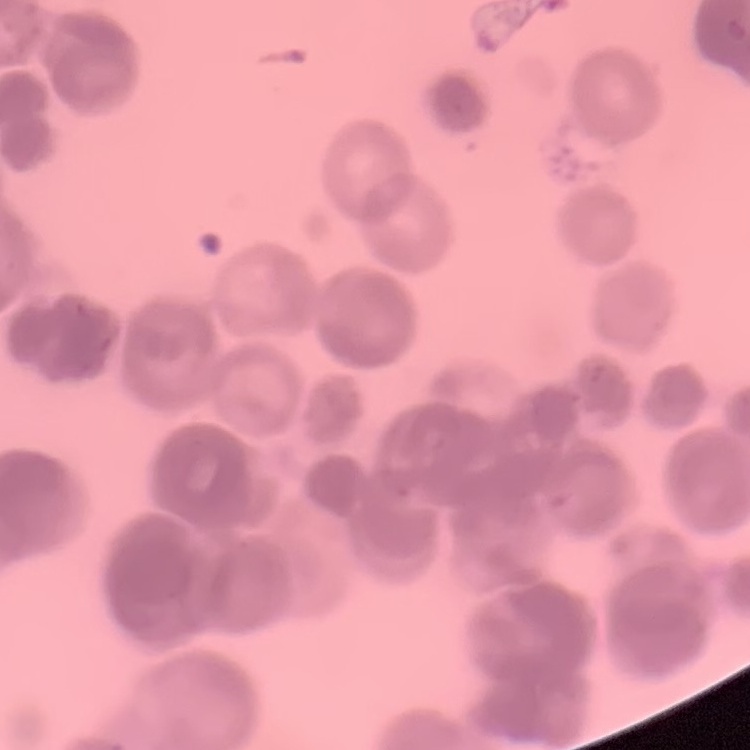

The erythrocytes show rouleaux formation. Thin peripheral smear. Square crop of a larger photomicrograph. Field's or Giemsa stain.